Report the malaria status of this cell.
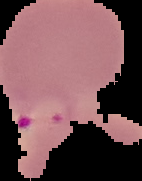
It is parasitized.

Image is 142×181 pixels. From a thin blood smear. The area outside the segmented cell region is set to black.